Classify this cell by malaria status.
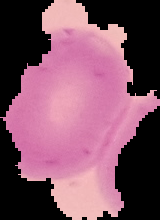
Uninfected.

Summary:
  - Preparation: thin blood smear
  - Image size: 160×220 pixels
  - Image type: segmented cell region on a black background